Locate every Plasmodium parasite.
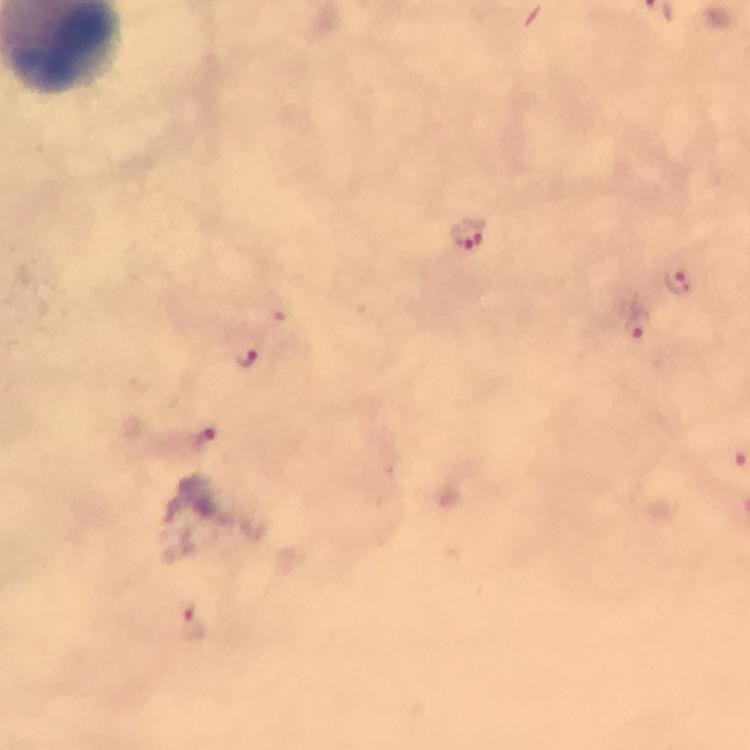

Approximate centers as [x, y] in pixels.
Plasmodium parasites: [467, 231], [678, 281], [636, 326], [247, 358], [203, 437], [191, 622].

Summary:
  - Capture: smartphone mounted on the microscope
  - Magnification: 100x
  - Context: from a diagnostic examination for malaria
  - Immersion oil: applied
  - Cropped from: one field of view
  - Preparation: thick smear
  - Image size: 750×750 pixels
  - Stain: Giemsa